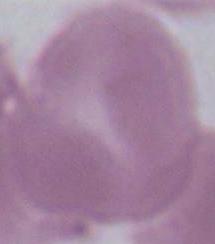
A red blood cell is seen. Photomicrograph. 1000x magnification.